Assess for parasitized red blood cells.
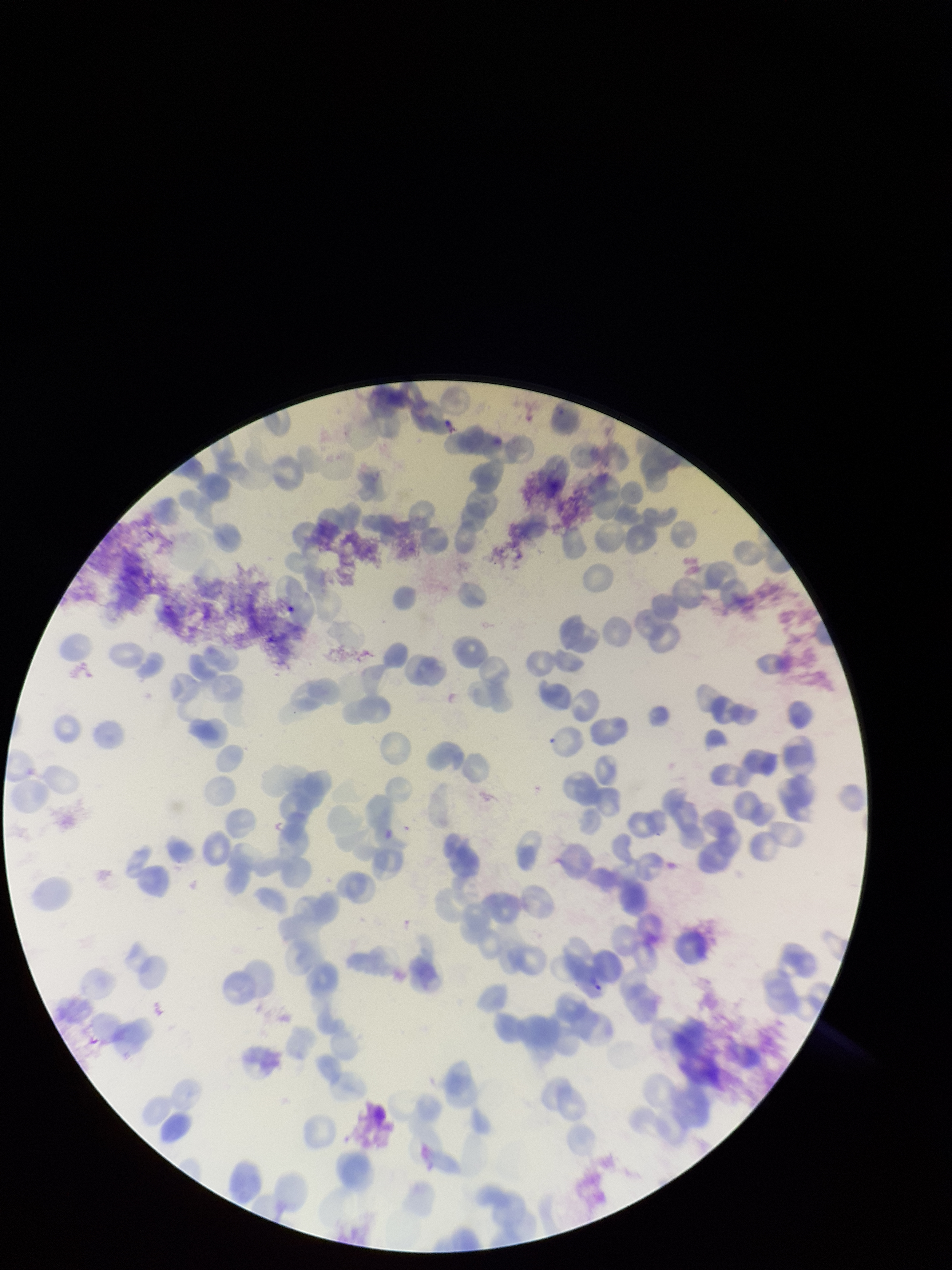
None seen.

Parasitized red blood cell count: 0. Image is 952×1270 pixels. Species reported for this patient: Plasmodium vivax. Photographed through the microscope eyepiece with a smartphone camera. Patient malaria status: infected. Giemsa stain. Preparation: thin blood smear. Red blood cell count: 153. One field from this slide.